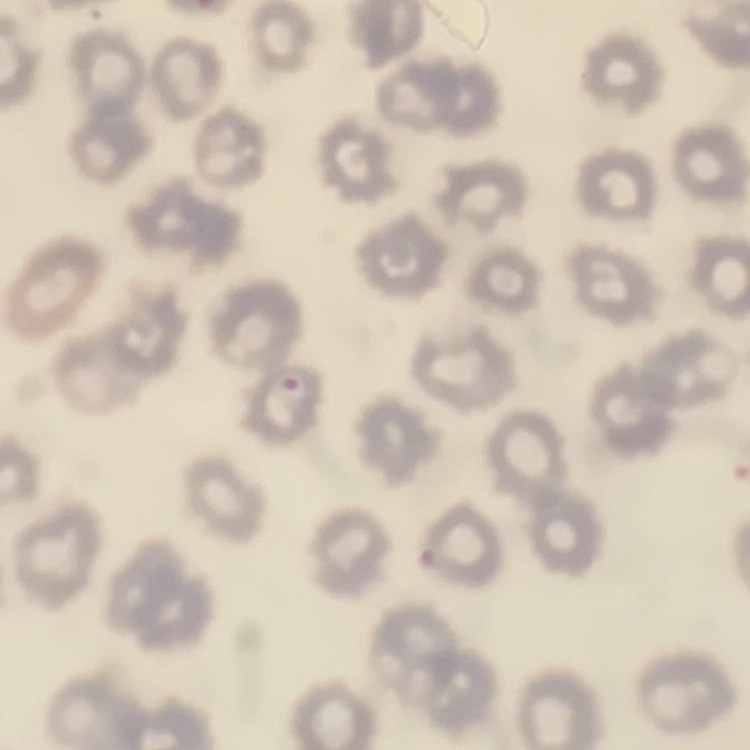
Summary:
  - Red blood cell morphology: no rouleaux formation
  - Preparation: thin blood film
  - Image type: square crop of a larger photomicrograph
  - Stain: Field's or Giemsa